Assess this cell for malaria.
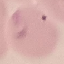
It is parasitized.

preparation = thin smear
stain = Giemsa
capture = smartphone camera at the microscope eyepiece
image type = cell patch, automatically extracted from a larger field of view and resized to 64 × 64 pixels